Assess this cell for malaria.
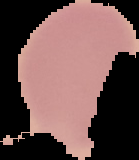

It is uninfected.

From a thin blood film. Image is 139×160 pixels. Segmented cell region on a black background.